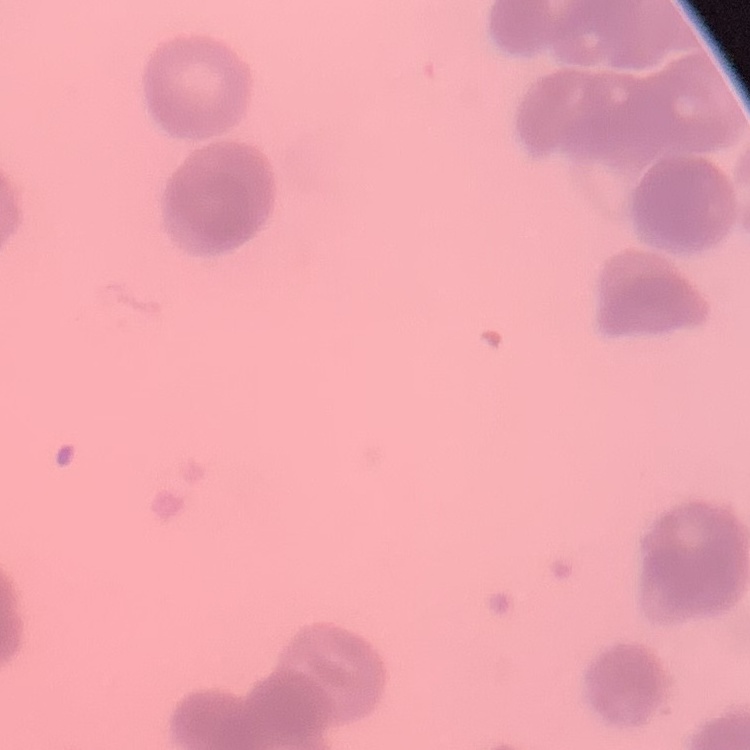

Summary:
  - Erythrocyte morphology: rouleaux formation
  - Stain: Field's or Giemsa
  - Image type: square crop of a larger photomicrograph
  - Preparation: thin blood smear